Assess the morphology of the erythrocytes.
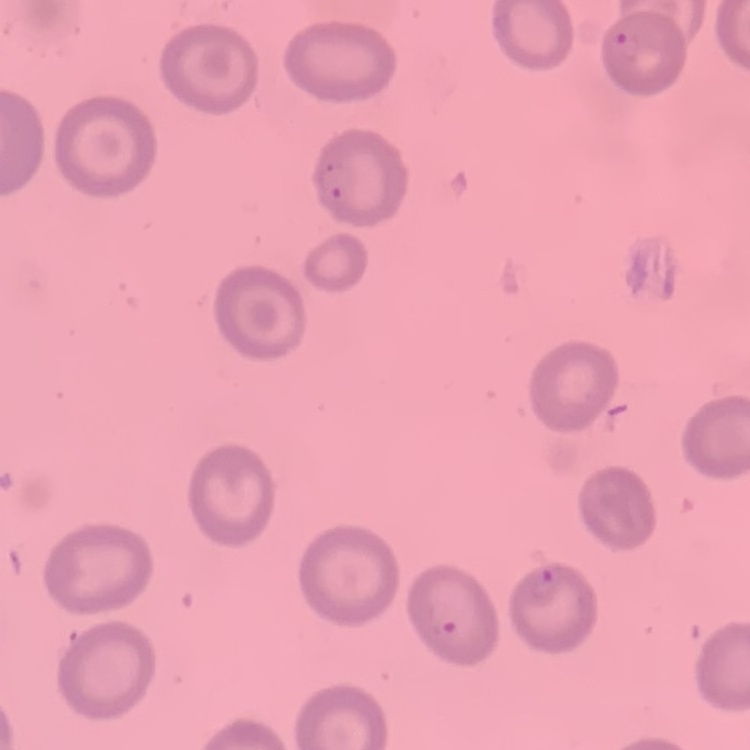
No rouleaux formation.

preparation: thin peripheral smear
stain: Field's or Giemsa
image_type: square crop of a larger photomicrograph